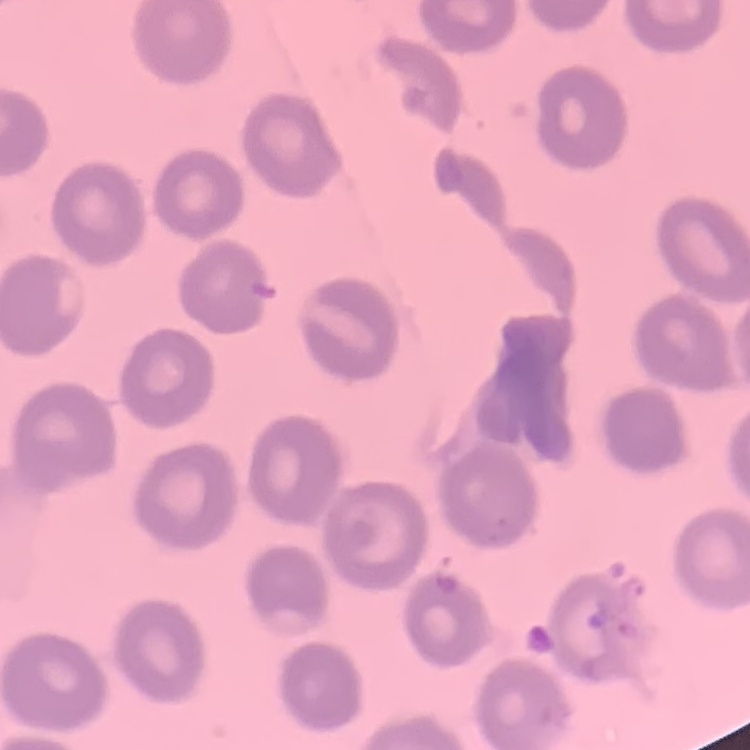

Summary:
  - Erythrocyte morphology: no rouleaux formation
  - Preparation: thin blood film
  - Image type: square crop of a larger photomicrograph
  - Stain: Field's or Giemsa